Outline each blood parasite and name the species.
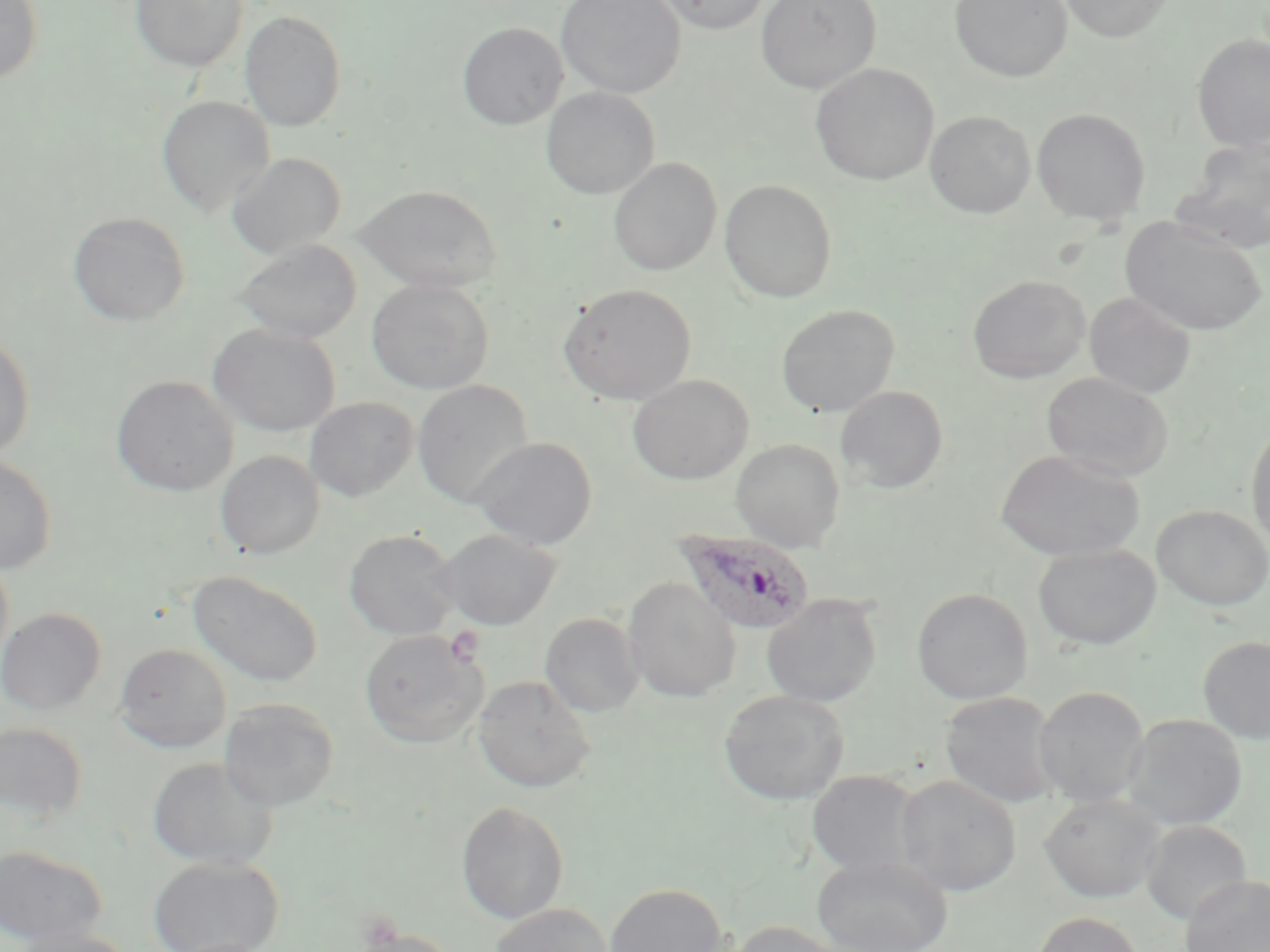

Approximate bounding boxes as [x1, y1, x2, y2] in pixels.
Plasmodium ovale-infected red blood cells: [674, 528, 815, 635].
No Plasmodium falciparum, Plasmodium malariae, Plasmodium vivax, Babesia divergens, or Trypanosoma brucei observed.

slide-level diagnosis = Plasmodium ovale
preparation = thin blood film
field of view = one of a larger specimen
stain = May-Grünwald-Giemsa
modality = optical microscopy
image size = 1270×952 pixels
platelet locations = approximate bounding boxes as [x1, y1, x2, y2] in pixels: [443, 625, 486, 667]
uninfected red blood cell locations = approximate bounding boxes as [x1, y1, x2, y2] in pixels: [0, 0, 43, 84], [555, 0, 686, 98], [650, 0, 773, 35], [756, 0, 881, 94], [949, 0, 1073, 82], [1057, 0, 1175, 43], [129, 1, 248, 72], [240, 10, 346, 131], [457, 22, 568, 130], [1191, 33, 1270, 152], [810, 63, 938, 185], [541, 87, 659, 199], [156, 95, 275, 217], [1031, 106, 1150, 225], [924, 110, 1036, 218], [1174, 139, 1269, 253], [226, 152, 346, 258], [608, 158, 722, 276], [719, 179, 837, 303], [355, 184, 502, 293], [68, 211, 190, 326], [1121, 216, 1268, 336], [236, 239, 361, 344], [968, 274, 1090, 384], [366, 278, 495, 394], [558, 283, 697, 405], [1084, 292, 1196, 399], [776, 304, 900, 417], [207, 323, 340, 437], [0, 332, 35, 463], [1041, 372, 1174, 482], [628, 374, 753, 485], [110, 375, 239, 496], [411, 379, 534, 508], [835, 385, 948, 493], [304, 396, 419, 502], [1246, 421, 1270, 552], [469, 436, 598, 551], [731, 438, 845, 552], [996, 449, 1145, 562], [215, 450, 325, 559], [0, 455, 58, 575], [1151, 505, 1270, 611], [436, 528, 561, 630], [343, 529, 462, 642], [1033, 542, 1161, 650], [0, 552, 14, 676], [187, 570, 325, 687], [623, 577, 740, 703], [911, 587, 1032, 705], [761, 595, 882, 707], [0, 607, 106, 715], [540, 612, 644, 717], [359, 629, 488, 748], [1198, 635, 1270, 744], [113, 642, 231, 752], [474, 674, 596, 793], [1034, 685, 1150, 807], [719, 690, 850, 805], [940, 691, 1062, 809], [219, 697, 340, 811], [1122, 713, 1247, 831], [0, 721, 89, 823], [147, 756, 278, 872], [806, 770, 925, 877], [893, 774, 1022, 897], [1039, 792, 1166, 903], [455, 800, 569, 924], [1140, 820, 1252, 926], [0, 844, 107, 949], [812, 854, 953, 952], [148, 855, 284, 952], [1179, 875, 1270, 952], [604, 882, 727, 952], [489, 903, 613, 952], [1033, 912, 1145, 952], [726, 920, 849, 952], [11, 926, 138, 952], [349, 927, 458, 952]
magnification = 1000x